Classify this cell by malaria status.
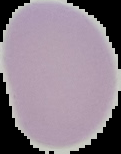
Uninfected.

From a thin blood smear. Image is 121×154 pixels. Segmented cell region on a black background.